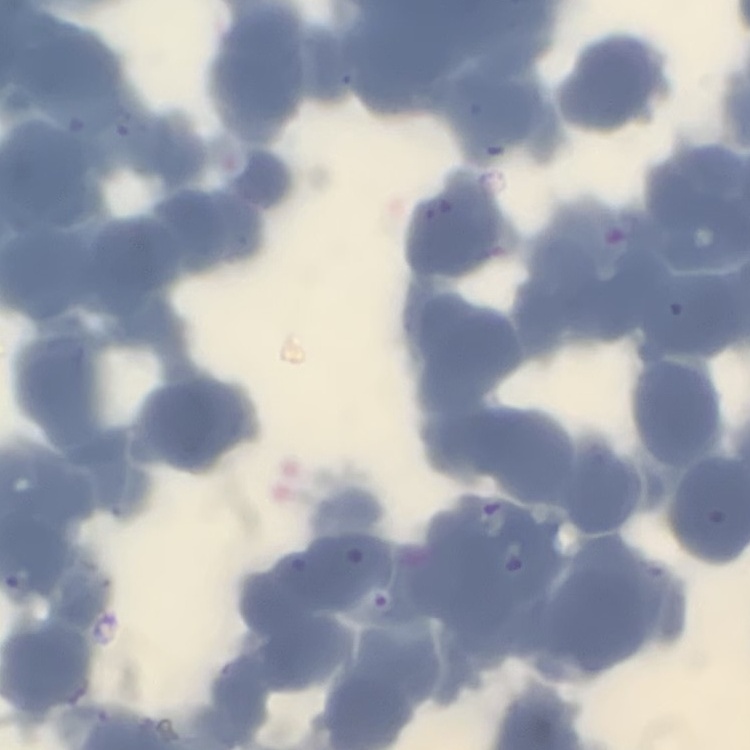

The erythrocytes show rouleaux formation. Thin blood smear. Field's or Giemsa stain. One tile cut from a larger photomicrograph.